Classify this cell by malaria status.
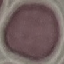

It is uninfected.

preparation = thin blood smear
stain = Giemsa
capture = smartphone through the microscope eyepiece
image type = automatically extracted cell patch, resized to 64 × 64 pixels